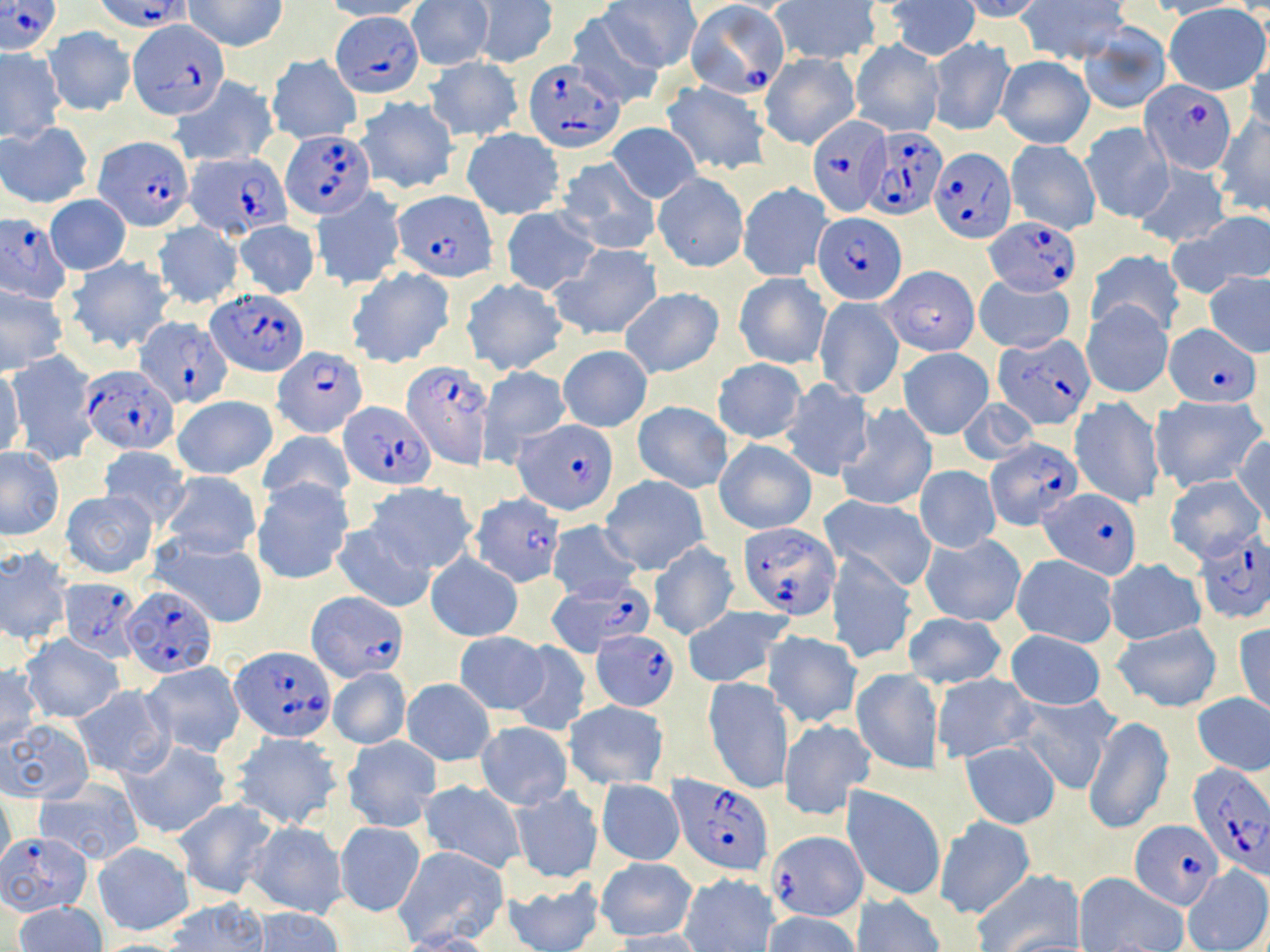

Approximate bounding boxes as [x1, y1, x2, y2] in pixels. Plasmodium falciparum-infected red blood cell locations: [98, 0, 189, 30], [1, 1, 61, 55], [685, 2, 791, 99], [332, 12, 424, 95], [128, 18, 226, 119], [522, 60, 624, 151], [1140, 80, 1238, 172], [806, 115, 890, 217], [864, 125, 948, 219], [282, 130, 374, 217], [95, 136, 192, 231], [931, 148, 1015, 245], [186, 151, 289, 237], [394, 190, 496, 281], [812, 213, 908, 305], [984, 215, 1081, 295], [1, 216, 70, 304], [206, 287, 309, 376], [136, 317, 231, 407], [1167, 323, 1261, 406], [993, 333, 1095, 429], [271, 346, 368, 437], [402, 355, 497, 467], [81, 367, 179, 454], [342, 401, 436, 488], [515, 422, 619, 515], [986, 437, 1081, 527], [1039, 486, 1140, 577], [468, 493, 565, 587], [735, 521, 839, 617], [1193, 533, 1269, 623], [59, 579, 140, 661], [547, 579, 653, 657], [123, 585, 216, 678], [306, 592, 408, 681], [591, 629, 680, 709], [231, 647, 334, 742], [1187, 764, 1270, 878], [669, 774, 775, 875], [1130, 818, 1222, 908], [1, 832, 92, 917], [765, 832, 867, 924]. Uninfected red blood cell locations: [185, 0, 288, 51], [323, 0, 427, 21], [408, 0, 493, 70], [470, 0, 558, 68], [601, 0, 701, 72], [884, 0, 980, 61], [961, 0, 1047, 22], [1019, 0, 1130, 64], [1145, 0, 1243, 20], [770, 1, 885, 62], [1164, 3, 1269, 94], [562, 10, 666, 108], [1079, 24, 1171, 114], [44, 27, 135, 116], [928, 37, 1015, 135], [851, 40, 943, 138], [1244, 48, 1270, 136], [0, 49, 65, 139], [760, 53, 860, 149], [995, 55, 1094, 149], [267, 56, 361, 143], [424, 57, 524, 141], [169, 76, 278, 167], [662, 79, 771, 175], [355, 96, 459, 195], [1213, 114, 1270, 216], [1082, 121, 1172, 224], [0, 122, 92, 207], [607, 122, 700, 203], [461, 129, 565, 220], [1006, 139, 1100, 235], [557, 157, 661, 256], [1133, 161, 1231, 248], [654, 173, 748, 271], [737, 182, 832, 281], [312, 186, 406, 291], [45, 196, 131, 274], [501, 206, 599, 295], [1179, 212, 1270, 293], [232, 219, 320, 299], [151, 222, 243, 309], [550, 243, 663, 341], [1084, 249, 1183, 338], [66, 255, 175, 355], [881, 265, 981, 356], [347, 266, 457, 367], [734, 272, 831, 370], [1204, 272, 1270, 357], [975, 274, 1074, 355], [460, 276, 568, 376], [0, 286, 67, 373], [620, 288, 723, 378], [814, 295, 903, 399], [1082, 299, 1173, 398], [558, 345, 652, 432], [898, 348, 994, 439], [6, 352, 98, 465], [712, 358, 807, 444], [477, 365, 572, 465], [0, 367, 25, 461], [777, 379, 874, 480], [172, 395, 277, 481], [1070, 395, 1164, 509], [1151, 395, 1265, 493], [958, 398, 1038, 466], [633, 401, 733, 491], [837, 404, 937, 512], [259, 428, 355, 509], [1231, 433, 1270, 524], [714, 438, 817, 534], [97, 446, 191, 529], [0, 449, 64, 539], [916, 465, 1000, 553], [160, 471, 263, 559], [1164, 473, 1267, 565], [600, 477, 708, 575], [252, 479, 353, 585], [366, 483, 476, 574], [62, 490, 158, 577], [820, 495, 939, 589], [545, 520, 639, 603], [332, 522, 435, 612], [149, 533, 270, 630], [921, 534, 1026, 627], [648, 542, 738, 640], [0, 548, 73, 646], [827, 550, 917, 665], [425, 553, 523, 642], [1012, 554, 1119, 647], [1106, 559, 1205, 645], [681, 606, 791, 688], [903, 612, 1007, 689], [1234, 623, 1270, 716], [1111, 624, 1224, 713], [1004, 629, 1106, 710], [764, 630, 861, 728], [453, 631, 549, 714], [20, 635, 123, 723], [1160, 636, 1268, 739], [507, 640, 591, 737], [139, 661, 246, 758], [0, 666, 41, 748], [327, 667, 410, 749], [852, 669, 942, 775], [931, 674, 1036, 763], [702, 677, 791, 796], [402, 678, 494, 765], [71, 686, 175, 779], [1193, 692, 1270, 777], [1015, 693, 1120, 794], [564, 701, 669, 789], [1084, 715, 1173, 835], [779, 717, 875, 820], [2, 719, 92, 801], [476, 722, 572, 809], [229, 733, 342, 831], [342, 736, 441, 832], [122, 740, 230, 839], [960, 740, 1062, 829], [598, 779, 683, 866], [419, 780, 526, 872], [34, 783, 144, 864], [842, 786, 946, 902], [509, 787, 602, 883], [0, 793, 15, 875], [173, 799, 277, 900], [935, 816, 1036, 920], [245, 822, 347, 918], [334, 822, 426, 917], [93, 841, 193, 935], [393, 845, 507, 946], [596, 857, 697, 942], [1182, 865, 1270, 951], [974, 870, 1084, 951], [679, 872, 780, 951], [1074, 873, 1189, 951], [502, 876, 603, 952], [850, 893, 946, 952], [163, 898, 269, 951], [13, 901, 106, 952], [249, 908, 344, 952], [762, 911, 861, 952], [608, 929, 710, 952], [398, 931, 499, 952]. Slide-level diagnosis: Plasmodium falciparum. 1000x magnification. Light microscopy. Single field of view. Image is 1270×952 pixels. Thin blood smear. May-Grünwald-Giemsa-stained preparation.